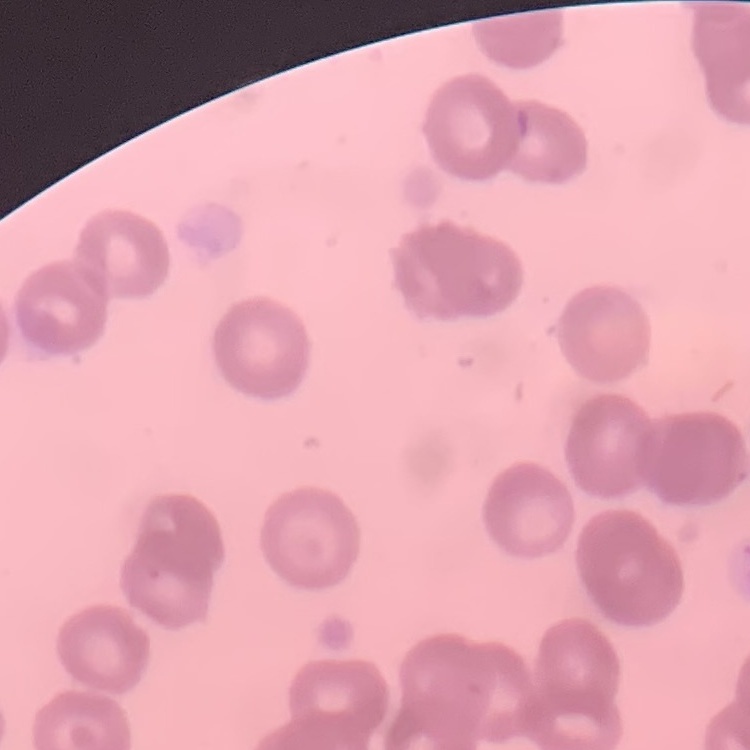

Summary:
  - Red blood cell morphology: rouleaux formation
  - Stain: Field's or Giemsa
  - Preparation: thin blood film
  - Image type: one tile cut from a larger photomicrograph